Draw a bounding box around every artifact (stain precipitate or debris).
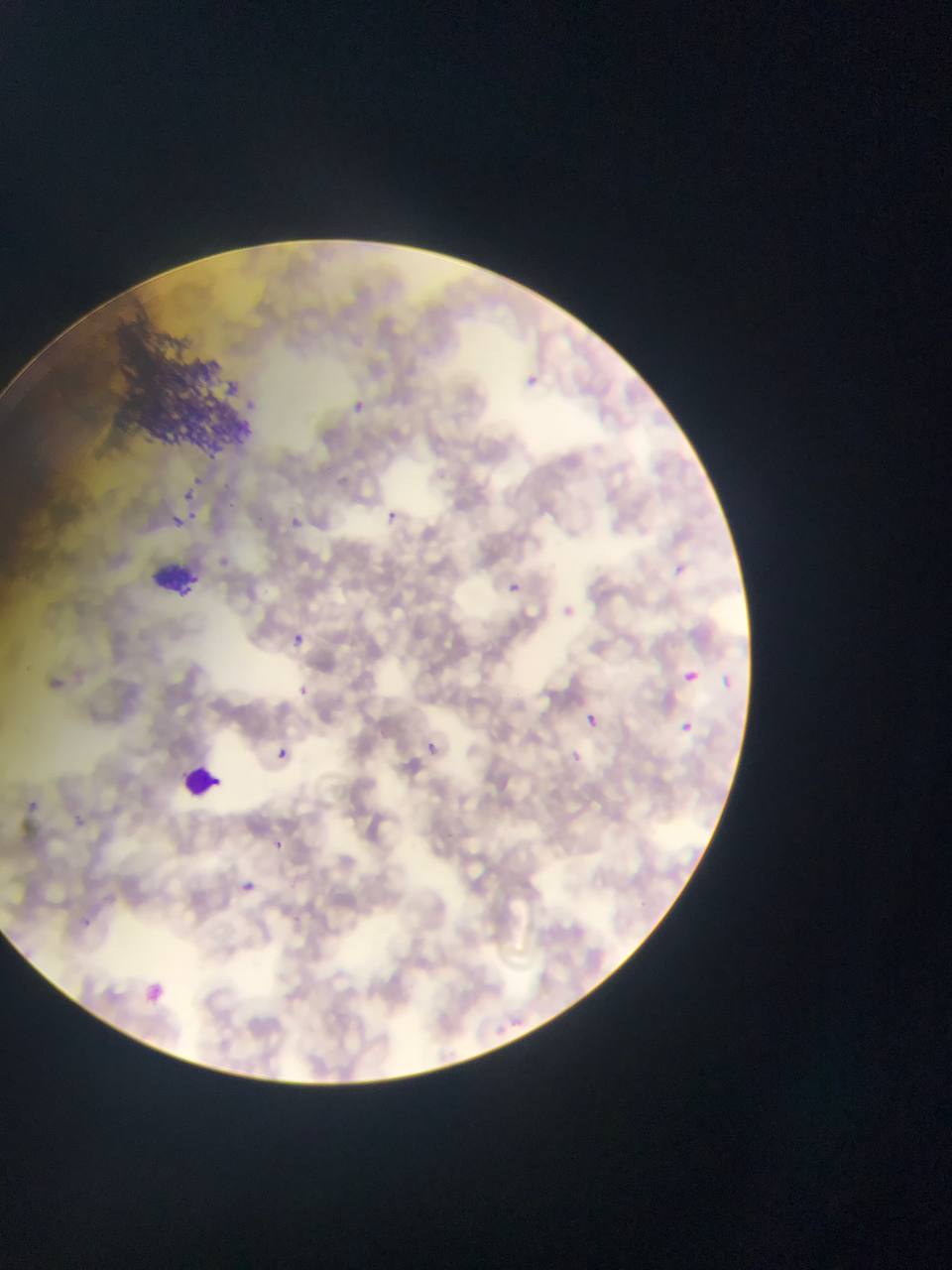
Approximate bounding boxes as {left, top, right, bottom} in pixels.
Artifacts (stain precipitate or debris): {99, 317, 263, 471}.

image size = 952×1270 pixels
country = Ghana
capture = mobile-phone photograph through a microscope
Plasmodium parasite locations = approximate bounding boxes as {left, top, right, bottom} in pixels: {519, 374, 538, 389}, {347, 398, 370, 417}, {182, 486, 201, 503}, {390, 509, 398, 525}, {190, 511, 194, 522}, {292, 511, 305, 529}, {172, 515, 181, 525}, {673, 563, 685, 580}, {506, 577, 526, 592}, {290, 628, 309, 651}, {679, 664, 705, 680}, {722, 673, 732, 698}, {298, 688, 313, 694}, {584, 713, 600, 739}, {680, 723, 695, 733}, {275, 744, 295, 760}, {23, 800, 41, 820}, {276, 841, 289, 853}, {242, 881, 260, 894}, {150, 982, 169, 1007} | approximate {x, y} pixel centers of objects too small to bound: {430, 746}
preparation = thin blood film
field of view = single
leukocyte locations = approximate bounding boxes as {left, top, right, bottom} in pixels: {134, 556, 200, 596}, {187, 755, 232, 805}